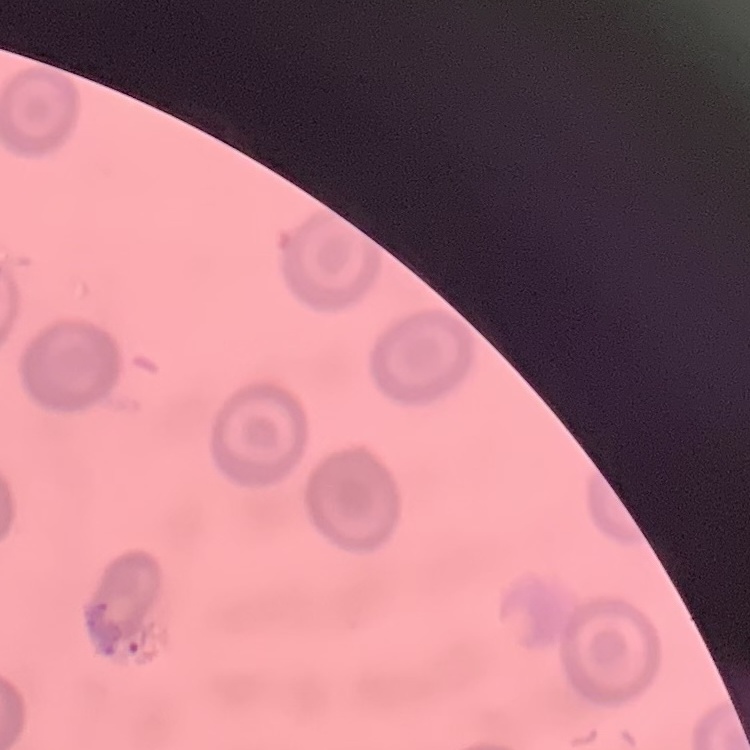
red blood cell morphology = no rouleaux formation
preparation = thin peripheral smear
stain = Field's or Giemsa
image type = square crop of a larger photomicrograph